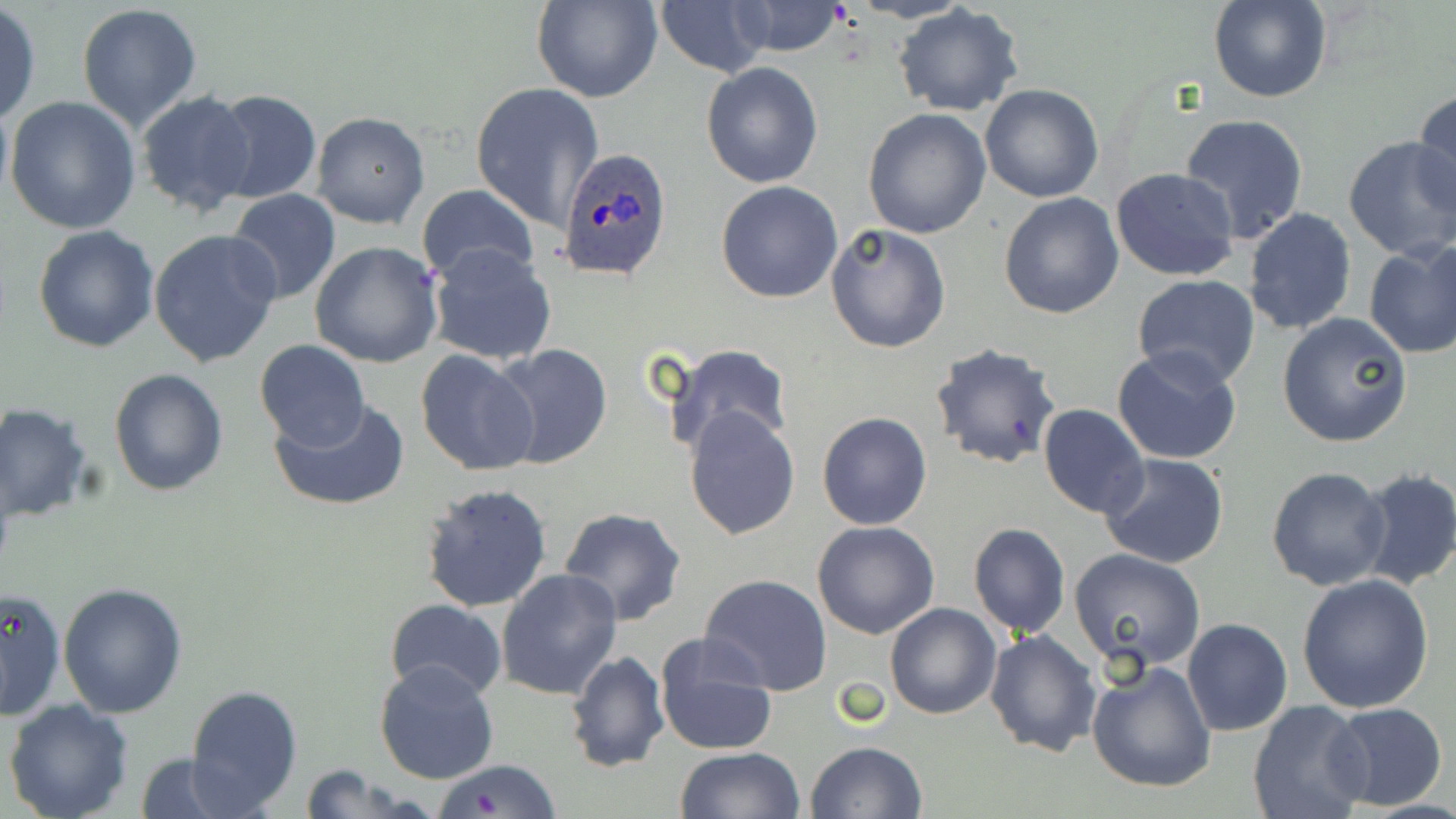
Summary:
  - Coordinate format: approximate bounding boxes as (x1, y1, x2, y2) in pixels
  - Uninfected red blood cell locations: (534, 0, 661, 103), (851, 0, 973, 24), (1207, 0, 1332, 103), (653, 2, 767, 76), (723, 2, 851, 57), (76, 4, 203, 132), (894, 4, 1024, 116), (0, 6, 41, 124), (701, 62, 823, 188), (470, 81, 604, 231), (980, 84, 1105, 202), (1411, 88, 1456, 221), (209, 89, 321, 205), (134, 90, 259, 216), (5, 95, 141, 234), (863, 109, 991, 239), (311, 110, 430, 230), (1179, 114, 1310, 243), (1342, 136, 1456, 262), (1110, 165, 1240, 281), (716, 180, 843, 302), (418, 184, 539, 290), (227, 190, 342, 306), (999, 192, 1123, 319), (1243, 208, 1356, 334), (825, 223, 950, 354), (33, 224, 160, 353), (149, 228, 282, 369), (310, 241, 443, 368), (1363, 241, 1456, 359), (428, 244, 557, 365), (1131, 274, 1260, 389), (1277, 312, 1413, 448), (254, 338, 370, 450), (661, 343, 794, 459), (488, 344, 613, 469), (929, 344, 1061, 470), (1112, 347, 1242, 465), (414, 349, 540, 478), (109, 368, 228, 498), (270, 398, 410, 512), (0, 402, 94, 522), (1039, 403, 1148, 519), (683, 405, 800, 540), (818, 412, 932, 530), (1098, 453, 1229, 570), (1267, 466, 1392, 590), (1354, 467, 1456, 591), (420, 482, 552, 612), (557, 506, 689, 627), (812, 521, 941, 639), (968, 522, 1070, 639), (1068, 549, 1207, 674), (495, 568, 622, 700), (698, 573, 833, 696), (1297, 573, 1434, 713), (59, 583, 189, 718), (0, 586, 65, 719), (385, 600, 509, 702), (884, 601, 1001, 719), (1182, 618, 1291, 737), (985, 628, 1102, 757), (652, 633, 779, 756), (564, 649, 669, 774), (1086, 659, 1218, 793), (373, 660, 500, 785), (184, 684, 302, 813), (4, 699, 135, 819), (1247, 700, 1372, 819), (1324, 702, 1448, 812), (806, 741, 928, 819), (675, 747, 804, 819), (132, 753, 247, 819), (432, 759, 562, 818), (293, 765, 429, 819)
  - Plasmodium ovale-infected red blood cell locations: (556, 145, 674, 282)
  - Slide-level diagnosis: Plasmodium ovale
  - Modality: optical microscopy
  - Image size: 1456×819 pixels
  - Field of view: one of a larger specimen
  - Magnification: 1000x
  - Preparation: thin blood film
  - Stain: May-Grünwald-Giemsa